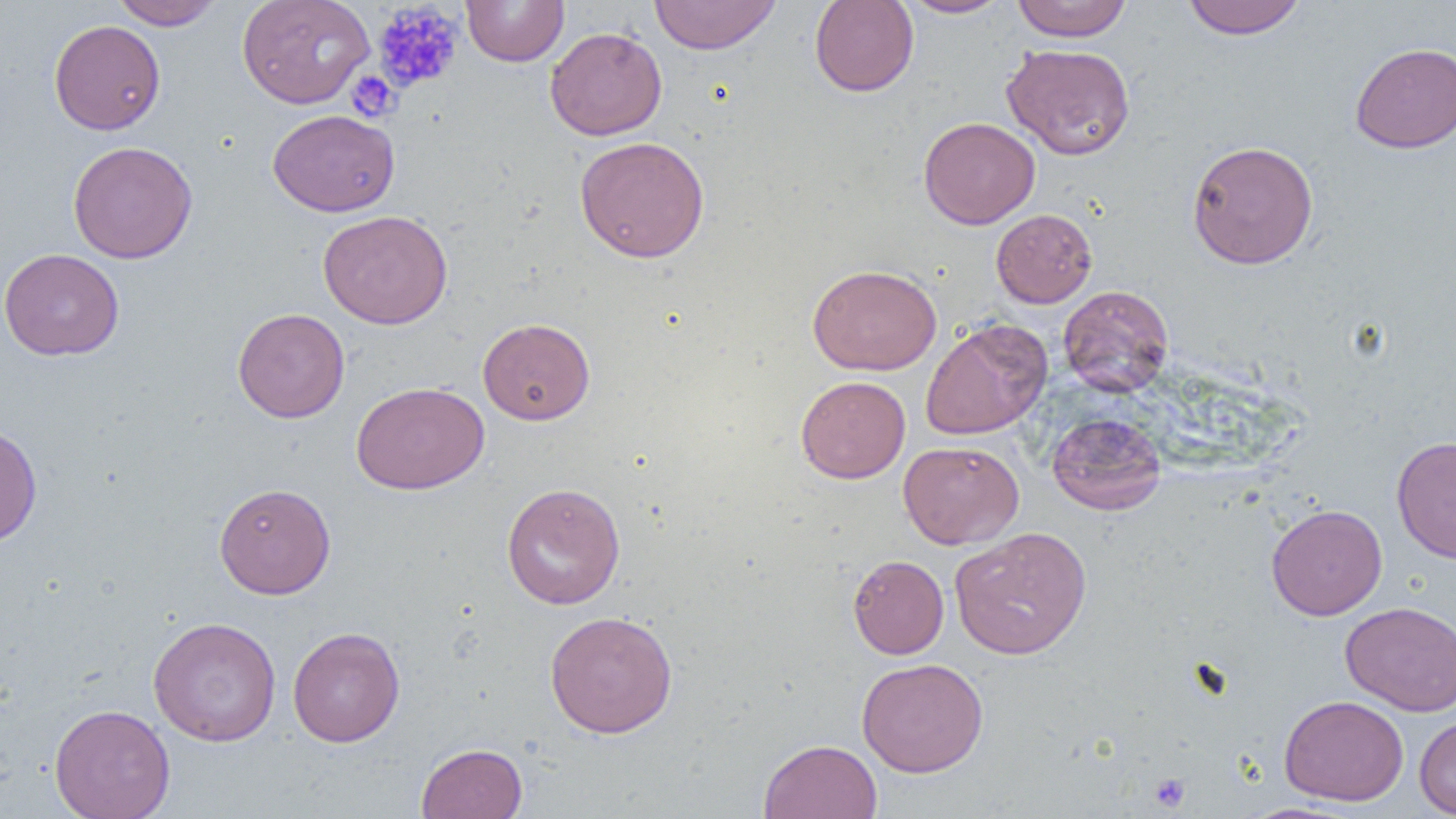

Summary:
  - Coordinate format: approximate bounding boxes as [x1, y1, x2, y2] in pixels
  - Uninfected red blood cell locations: [110, 0, 223, 30], [237, 0, 374, 109], [460, 0, 570, 67], [648, 0, 782, 54], [809, 0, 919, 97], [897, 0, 1012, 18], [1012, 0, 1132, 42], [1181, 0, 1307, 39], [49, 20, 165, 135], [544, 26, 667, 140], [1350, 42, 1456, 153], [1001, 43, 1136, 160], [267, 109, 399, 217], [918, 116, 1040, 229], [574, 136, 710, 263], [1186, 139, 1319, 269], [67, 140, 197, 264], [991, 209, 1097, 308], [318, 210, 453, 329], [0, 247, 124, 360], [807, 264, 942, 375], [1058, 284, 1174, 397], [232, 307, 349, 423], [478, 317, 595, 425], [920, 318, 1052, 440], [795, 376, 910, 483], [351, 381, 489, 495], [1046, 412, 1167, 515], [0, 423, 43, 547], [1391, 436, 1456, 563], [898, 440, 1024, 549], [501, 482, 626, 610], [214, 483, 336, 599], [1266, 503, 1387, 620], [950, 526, 1092, 659], [847, 554, 949, 659], [1340, 601, 1456, 716], [544, 610, 678, 738], [148, 616, 281, 746], [287, 626, 405, 747], [856, 658, 988, 778], [1279, 694, 1409, 806], [49, 703, 175, 819], [1414, 714, 1456, 817], [759, 738, 882, 818], [416, 742, 527, 818]
  - Platelet locations: [371, 2, 465, 93], [346, 70, 401, 122], [1148, 773, 1190, 812]
  - Slide-level diagnosis: no evidence of blood parasites
  - Image size: 1456×819 pixels
  - Magnification: 1000x
  - Preparation: thin blood smear
  - Modality: light microscopy
  - Field of view: single